State the preparation type.
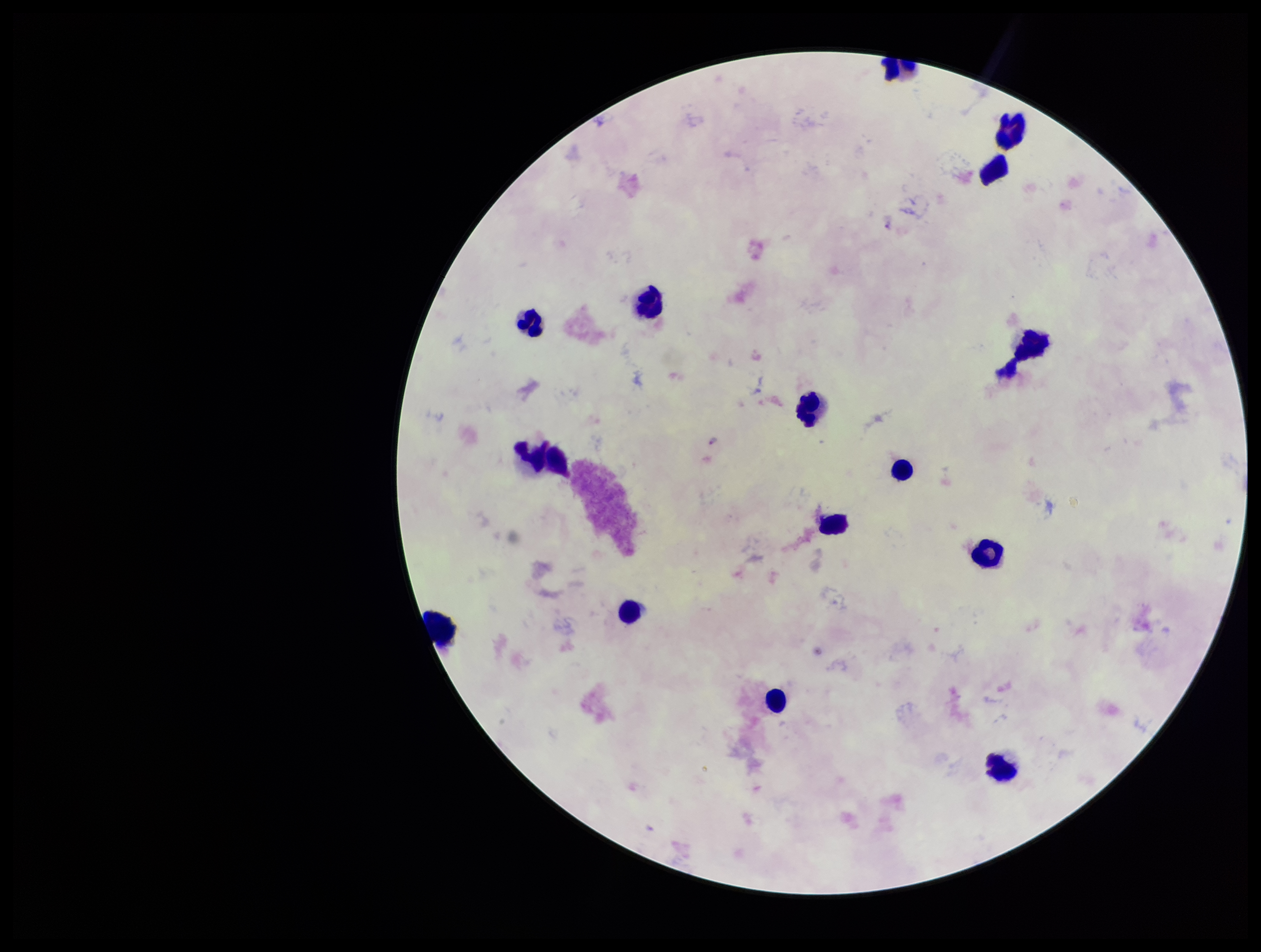

A thick smear.

Summary:
  - Capture: smartphone photograph through the microscope eyepiece
  - Leukocyte count: 15
  - Patient malaria status: infected
  - Stain: Giemsa
  - Plasmodium parasites: detected
  - Field of view: single
  - Image size: 1261×952 pixels
  - Species reported for this patient: Plasmodium falciparum
  - Parasite count: 2